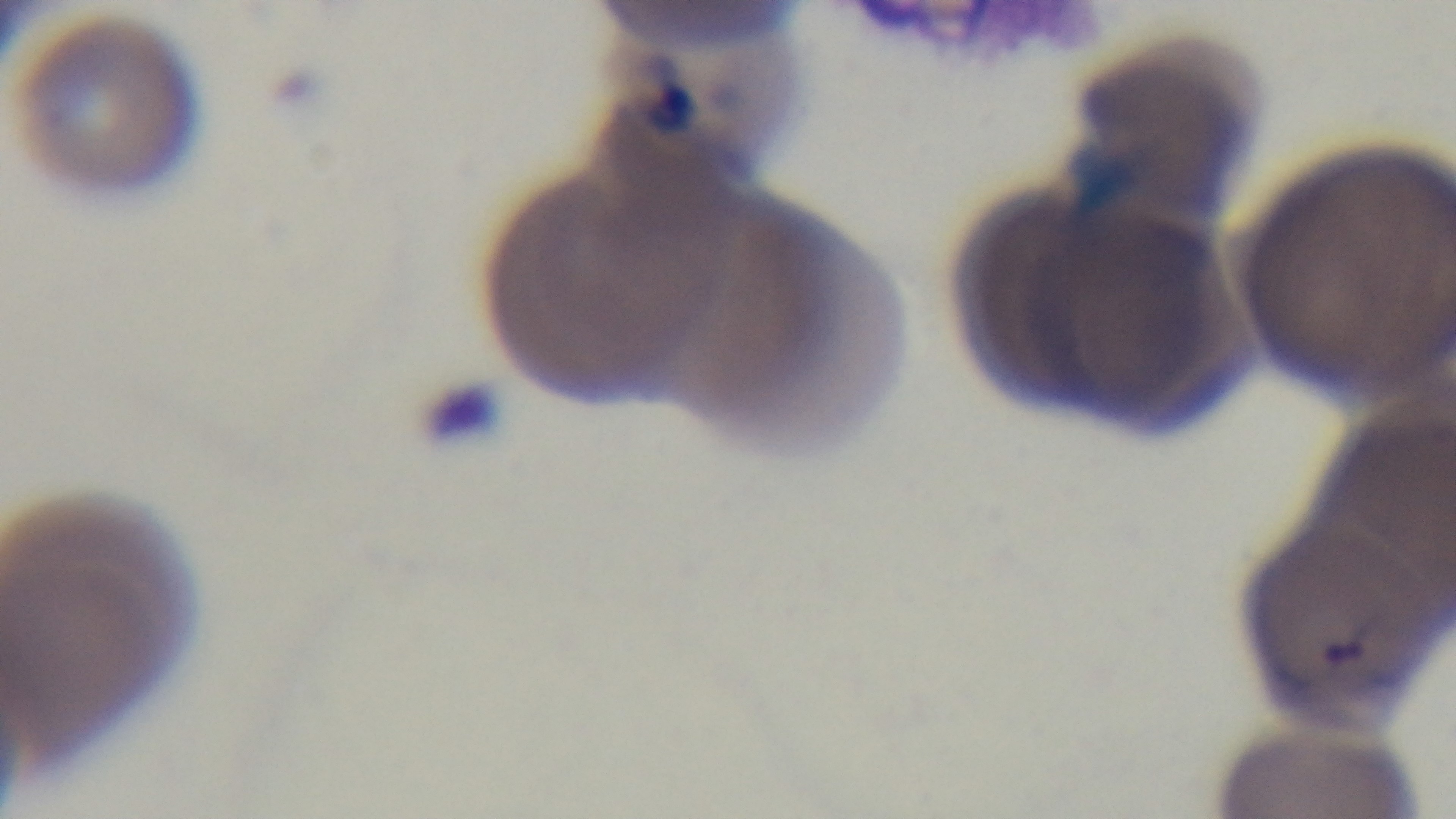
Summary:
  - Stain: Giemsa
  - Modality: light microscopy
  - Field of view: one from the slide
  - Malaria status: infected
  - Objective: 100x oil immersion
  - Preparation: thin blood film
  - Capture: mounted 4K digital camera